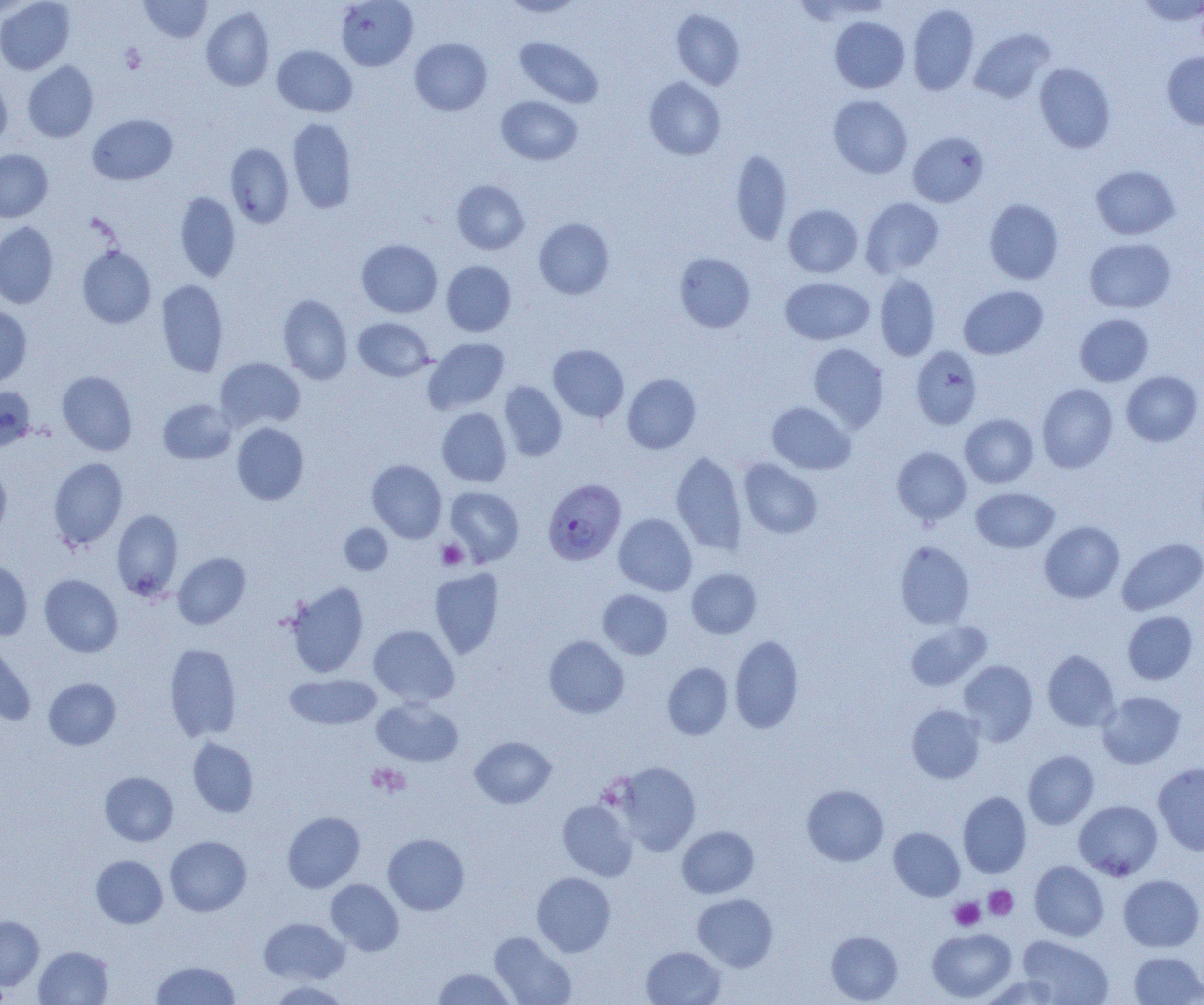

slide-level diagnosis = Plasmodium falciparum
preparation = thin blood film
magnification = 1000x
uninfected red blood cell locations = approximate bounding boxes as (x1, y1, x2, y2) in pixels: (138, 0, 212, 43), (0, 1, 75, 74), (336, 1, 418, 71), (499, 1, 586, 17), (1137, 1, 1203, 24), (907, 4, 979, 95), (200, 7, 274, 91), (671, 8, 745, 90), (830, 16, 910, 93), (969, 28, 1054, 104), (514, 36, 605, 108), (409, 38, 492, 116), (272, 45, 357, 117), (1162, 52, 1204, 130), (23, 60, 99, 143), (1034, 63, 1116, 153), (0, 77, 12, 150), (644, 77, 726, 160), (828, 95, 913, 178), (497, 96, 582, 165), (87, 114, 178, 185), (287, 117, 357, 213), (907, 131, 989, 208), (225, 143, 294, 228), (0, 149, 53, 222), (731, 149, 793, 245), (1091, 165, 1179, 239), (451, 180, 529, 255), (175, 192, 240, 282), (861, 197, 944, 277), (984, 199, 1064, 284), (783, 204, 863, 278), (534, 218, 614, 300), (0, 222, 58, 309), (1084, 238, 1176, 312), (356, 239, 443, 317), (77, 246, 156, 328), (674, 252, 755, 332), (441, 261, 516, 337), (875, 274, 941, 361), (780, 277, 874, 345), (156, 279, 228, 377), (958, 285, 1048, 359), (278, 294, 353, 384), (0, 305, 32, 387), (1074, 313, 1154, 386), (352, 317, 434, 382), (424, 337, 510, 413), (808, 343, 889, 431), (547, 344, 629, 423), (911, 345, 983, 429), (215, 357, 305, 431), (1121, 370, 1202, 447), (57, 371, 137, 455), (622, 374, 701, 453), (499, 381, 567, 461), (1037, 383, 1118, 473), (0, 385, 36, 451), (158, 399, 236, 464), (766, 401, 855, 474), (437, 407, 511, 487), (960, 413, 1038, 488), (232, 423, 309, 505), (892, 446, 971, 525), (670, 450, 748, 555), (48, 457, 128, 549), (739, 459, 822, 539), (367, 460, 447, 542), (0, 463, 11, 541), (445, 486, 524, 566), (971, 487, 1059, 553), (112, 509, 183, 600), (613, 513, 697, 595), (1039, 521, 1124, 603), (339, 523, 392, 575), (1117, 538, 1204, 615), (895, 541, 974, 629), (173, 552, 250, 629), (0, 559, 32, 641), (429, 568, 504, 658), (686, 568, 762, 638), (39, 574, 123, 657), (285, 580, 369, 678), (598, 589, 672, 659), (1122, 611, 1198, 685), (905, 620, 991, 691), (368, 624, 459, 705), (544, 635, 629, 718), (729, 635, 804, 733), (0, 638, 36, 725), (165, 643, 241, 742), (1042, 650, 1119, 731), (957, 659, 1038, 745), (663, 662, 732, 740), (285, 674, 382, 730), (44, 678, 121, 750), (1097, 691, 1185, 769), (372, 697, 463, 767), (906, 705, 985, 783), (470, 736, 556, 808), (188, 737, 258, 817), (1023, 750, 1099, 829), (614, 762, 701, 855), (1153, 763, 1204, 855), (100, 771, 178, 846), (802, 784, 889, 866), (958, 791, 1031, 878), (1074, 799, 1162, 880), (557, 800, 637, 881), (282, 811, 365, 892), (677, 826, 759, 898), (889, 827, 965, 901), (383, 833, 469, 915), (165, 836, 251, 916), (91, 855, 168, 928), (1030, 860, 1109, 940), (532, 872, 615, 956), (1118, 874, 1204, 951), (326, 879, 404, 956), (692, 893, 778, 971), (0, 916, 44, 991), (259, 917, 349, 984), (928, 927, 1016, 1002), (825, 930, 903, 1004), (489, 931, 576, 1005), (1018, 936, 1112, 1004), (34, 946, 113, 1004), (642, 946, 725, 1005), (1129, 951, 1203, 1004), (151, 960, 240, 1005), (433, 967, 516, 1004), (978, 974, 1063, 1004), (266, 980, 351, 1005)
image size = 1204×1005 pixels
field of view = single
Plasmodium falciparum-infected red blood cell locations = approximate bounding boxes as (x1, y1, x2, y2) in pixels: (543, 479, 627, 566)
platelet locations = approximate bounding boxes as (x1, y1, x2, y2) in pixels: (119, 44, 147, 74), (436, 539, 467, 570), (368, 764, 410, 797), (984, 885, 1018, 920), (949, 897, 985, 931)
modality = light microscopy